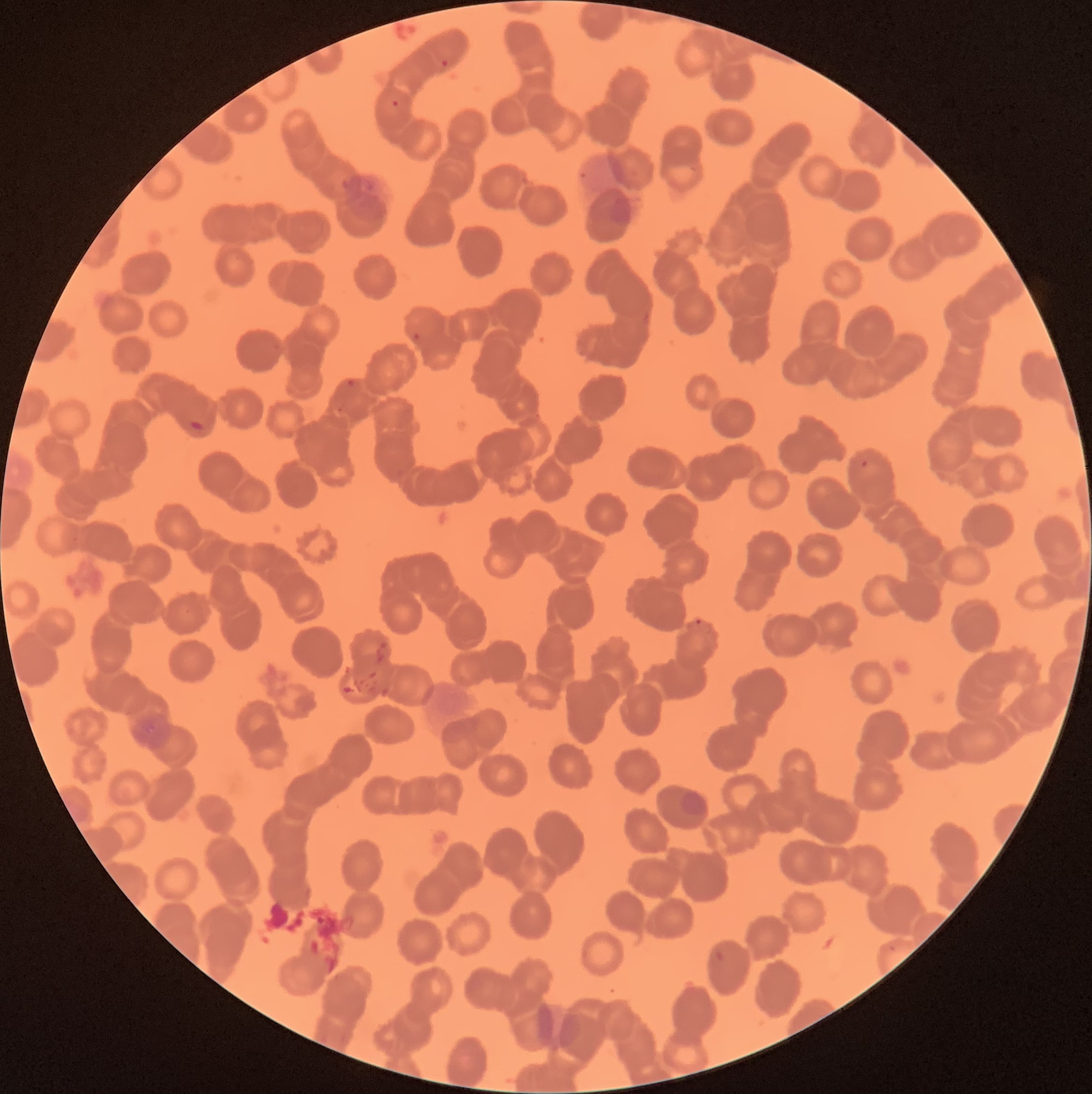

preparation: thin blood film
red_blood_cell_morphology: rouleaux formation
image_size: 1092×1094 pixels
modality: optical microscopy
plasmodium_parasite_locations: 'approximate bounding boxes as [x1, y1, x2, y2] in pixels: [440, 58, 450, 68], [391, 99, 400, 108], [413, 332, 420, 340], [346, 378, 357, 388], [189, 420, 204, 432], [861, 459, 869, 468], [694, 618, 702, 627]'
plasmodium_parasites_too_small_for_a_box: 'approximate centers as [x, y] in pixels: [340, 409]'